Classify this cell by malaria status.
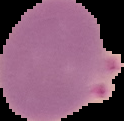

It is parasitized.

{
  "image_type": "segmented cell region with the area outside set to black",
  "preparation": "thin blood film",
  "image_size": "124×121 pixels"
}